Identify the blood parasite species.
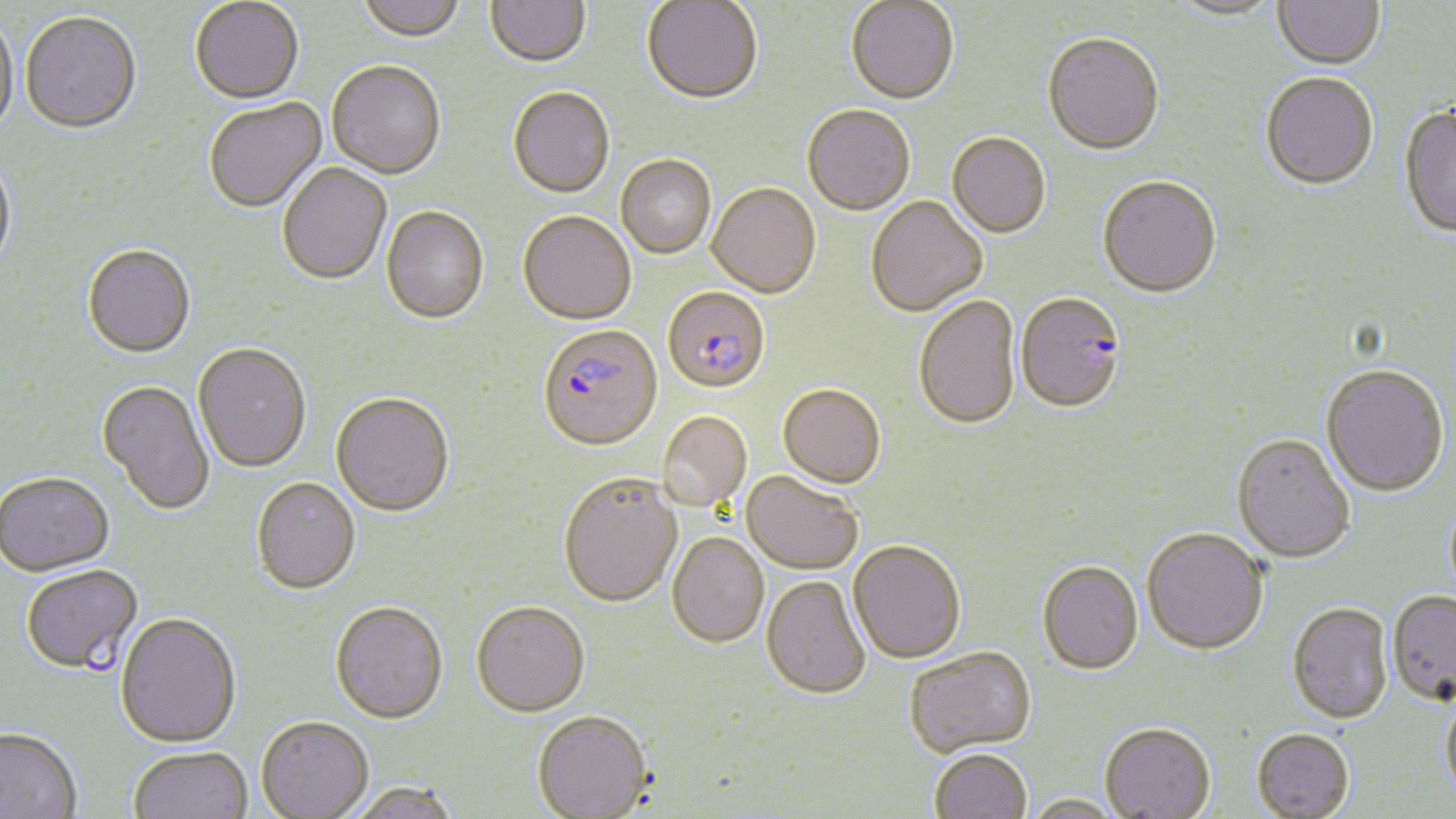
Plasmodium falciparum.

Summary:
  - Coordinate format: approximate bounding boxes as [x1, y1, x2, y2] in pixels
  - Plasmodium falciparum-infected red blood cell locations: [663, 288, 770, 395], [1015, 294, 1126, 416], [537, 325, 663, 453], [21, 566, 144, 678]
  - Uninfected red blood cell locations: [356, 0, 466, 45], [485, 0, 590, 70], [1273, 0, 1385, 71], [190, 1, 304, 107], [642, 1, 762, 107], [846, 1, 959, 107], [1165, 1, 1283, 22], [0, 14, 19, 143], [20, 14, 142, 137], [1042, 35, 1164, 158], [327, 63, 446, 181], [1260, 73, 1378, 191], [508, 89, 615, 200], [205, 99, 327, 215], [1399, 105, 1456, 240], [802, 107, 915, 217], [947, 134, 1050, 240], [0, 156, 16, 278], [616, 156, 716, 260], [277, 164, 392, 286], [1097, 178, 1222, 300], [706, 185, 821, 300], [866, 198, 987, 318], [381, 208, 489, 326], [518, 214, 636, 328], [82, 247, 195, 361], [914, 297, 1021, 432], [193, 345, 311, 475], [1321, 366, 1449, 499], [96, 382, 215, 516], [778, 385, 886, 490], [331, 395, 454, 520], [657, 412, 751, 512], [1231, 434, 1355, 565], [740, 472, 862, 575], [0, 474, 114, 579], [558, 476, 682, 610], [251, 480, 360, 597], [1142, 528, 1268, 656], [667, 534, 769, 649], [848, 542, 966, 665], [1037, 562, 1143, 677], [761, 576, 870, 701], [1386, 591, 1456, 708], [1287, 602, 1393, 724], [330, 604, 448, 727], [472, 604, 590, 721], [115, 615, 242, 750], [904, 649, 1037, 760], [1441, 692, 1456, 805], [532, 713, 652, 819], [256, 719, 374, 819], [1100, 725, 1216, 819], [1251, 728, 1354, 819], [0, 729, 82, 819], [128, 748, 252, 819], [929, 750, 1032, 819], [348, 785, 461, 819], [1022, 796, 1124, 819]
  - Modality: optical microscopy
  - Magnification: 1000x
  - Stain: May-Grünwald-Giemsa
  - Field of view: single
  - Image size: 1456×819 pixels
  - Preparation: thin blood smear